Classify this cell by malaria status.
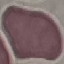
It is uninfected.

Summary:
  - Preparation: thin smear
  - Image type: cell patch, automatically extracted from a larger field of view and resized to 64 × 64 pixels
  - Capture: smartphone through the microscope eyepiece
  - Stain: Giemsa